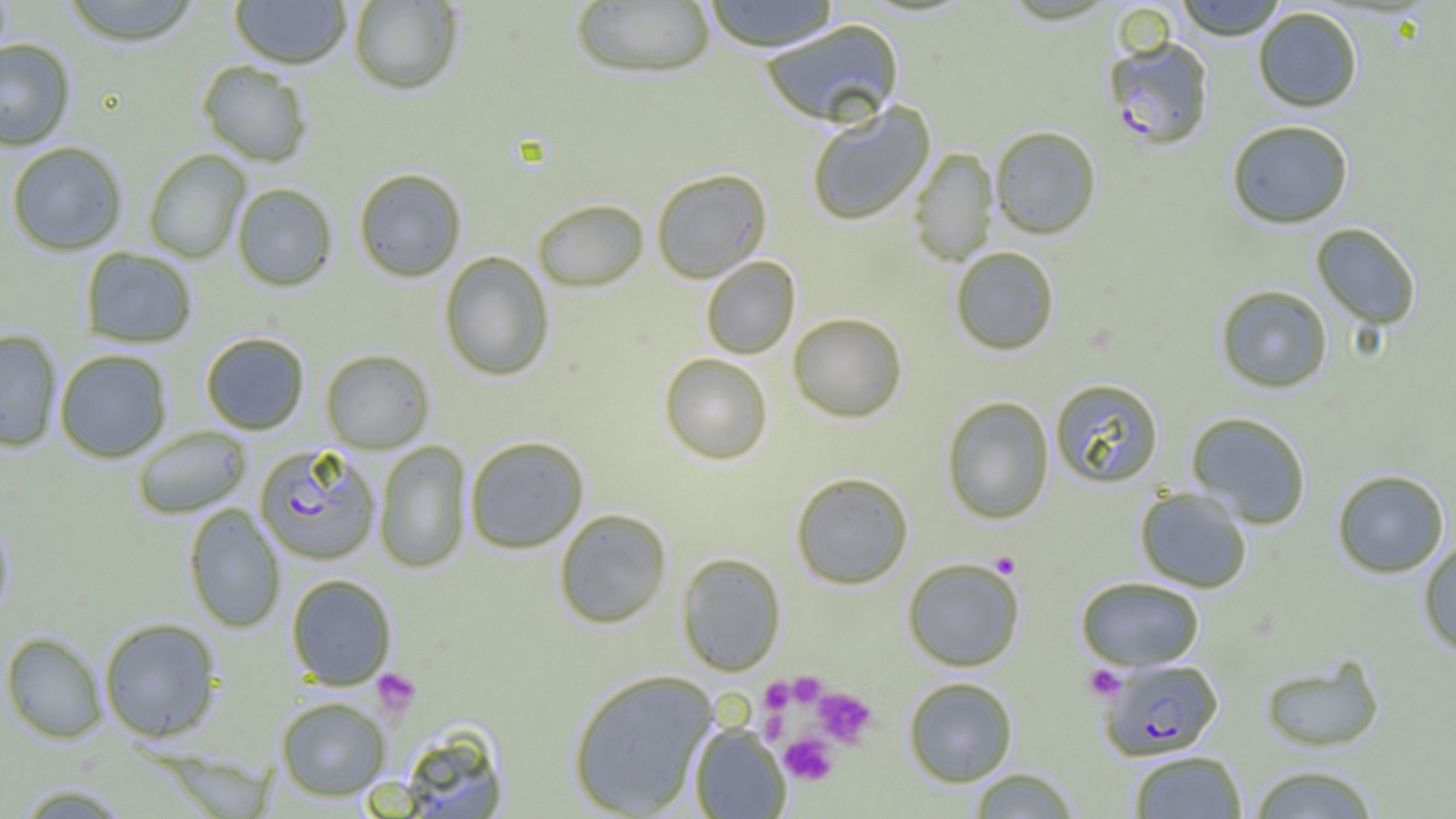

plasmodium_falciparum_infected_red_blood_cell_locations: 'approximate bounding boxes as (x1, y1, x2, y2) in pixels: (1104, 36, 1215, 149), (254, 444, 381, 564), (1099, 658, 1223, 760)'
slide_level_diagnosis: Plasmodium falciparum
preparation: thin blood film
modality: light microscopy
image_size: 1456×819 pixels
uninfected_red_blood_cell_locations: 'approximate bounding boxes as (x1, y1, x2, y2) in pixels: (61, 0, 202, 46), (229, 0, 352, 69), (348, 0, 464, 95), (701, 0, 841, 52), (1174, 0, 1289, 40), (570, 1, 716, 78), (1252, 6, 1363, 112), (758, 19, 905, 128), (0, 38, 75, 151), (197, 60, 313, 167), (805, 102, 935, 226), (1226, 120, 1354, 229), (990, 125, 1102, 239), (5, 141, 128, 256), (909, 148, 998, 266), (142, 149, 250, 263), (353, 167, 467, 282), (651, 168, 772, 283), (231, 182, 338, 291), (532, 198, 649, 292), (1311, 223, 1422, 330), (950, 246, 1060, 356), (80, 247, 198, 348), (439, 251, 555, 381), (701, 256, 800, 359), (1215, 285, 1333, 393), (787, 312, 908, 423), (0, 329, 62, 452), (200, 331, 310, 435), (320, 348, 435, 453), (53, 349, 173, 463), (659, 353, 773, 465), (1049, 378, 1165, 489), (941, 396, 1054, 524), (1186, 412, 1312, 529), (132, 426, 252, 519), (465, 436, 589, 554), (374, 440, 472, 574), (1332, 469, 1449, 578), (790, 471, 914, 589), (1135, 487, 1252, 593), (183, 502, 286, 634), (0, 507, 16, 627), (553, 508, 673, 629), (1417, 538, 1456, 657), (676, 552, 786, 676), (902, 557, 1026, 671), (285, 573, 397, 689), (1076, 576, 1205, 670), (98, 617, 223, 743), (2, 631, 108, 743), (1259, 654, 1386, 752), (567, 668, 718, 817), (903, 677, 1018, 787), (275, 696, 391, 800), (689, 723, 791, 818), (395, 727, 509, 819), (1128, 750, 1247, 818), (1248, 764, 1381, 818), (968, 767, 1080, 818), (11, 782, 132, 818)'
platelet_locations: 'approximate bounding boxes as (x1, y1, x2, y2) in pixels: (990, 551, 1022, 578), (1085, 665, 1125, 700), (371, 667, 421, 718), (788, 672, 827, 708), (760, 677, 796, 714), (813, 687, 877, 748), (760, 710, 789, 743), (780, 733, 837, 786)'
magnification: 1000x
field_of_view: one of a larger specimen